State the preparation type.
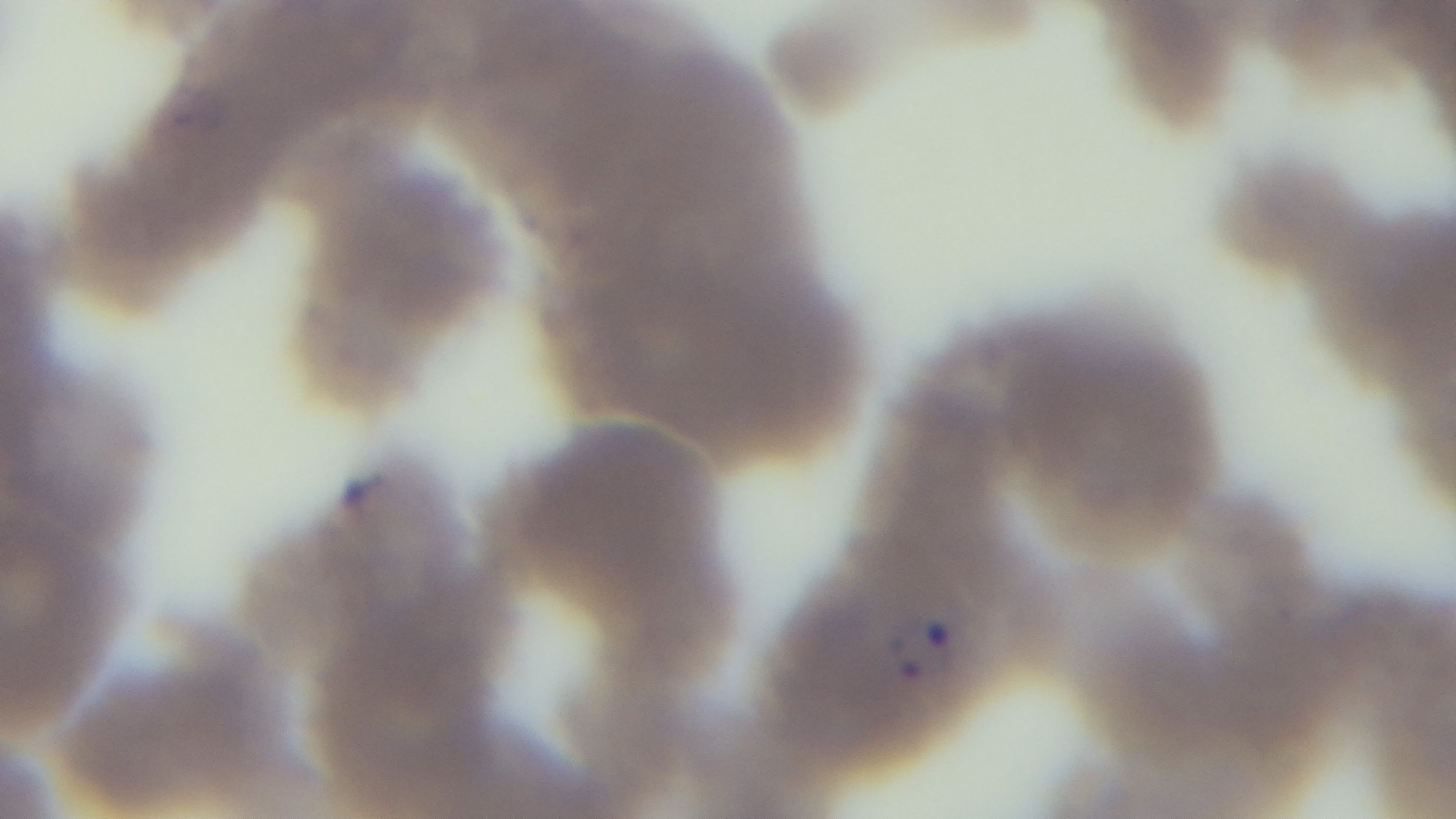

A thin smear.

Light microscopy. Mounted 4K digital camera. Malaria status: positive. 100x oil-immersion objective. One field from the slide. Giemsa-stained.